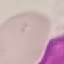

{
  "malaria_status": "uninfected",
  "stain": "Giemsa",
  "capture": "smartphone camera at the microscope eyepiece",
  "preparation": "thin smear",
  "image_type": "cell patch, automatically extracted from a larger field of view and resized to 64 × 64 pixels"
}